Report the malaria status of this cell.
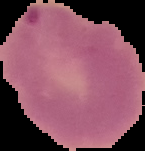

Parasitized.

image type = segmented cell region with the area outside set to black
preparation = thin blood film
image size = 145×151 pixels